Locate every blood parasite and identify its species.
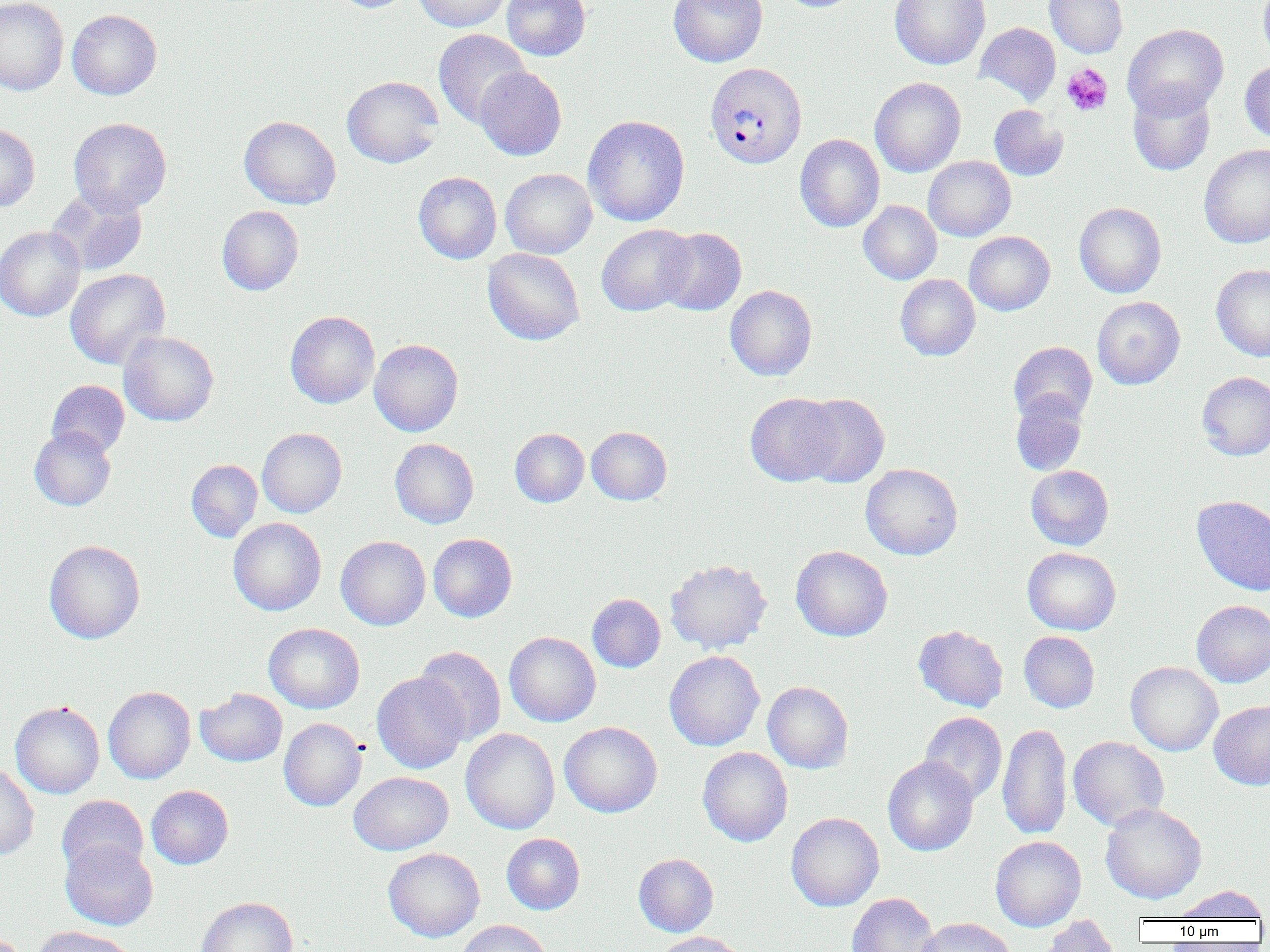

Approximate bounding boxes as named x1/y1/x2/y2 corners in pixels.
Plasmodium vivax-infected red blood cells: (x1=704, y1=62, x2=807, y2=170).
No Plasmodium falciparum, Plasmodium ovale, Plasmodium malariae, Babesia divergens, or Trypanosoma brucei observed.

slide-level diagnosis = Plasmodium vivax
field of view = single
platelet locations = approximate bounding boxes as named x1/y1/x2/y2 corners in pixels: (x1=1061, y1=63, x2=1113, y2=116)
preparation = thin blood film
modality = optical microscopy
magnification = 1000x
image size = 1270×952 pixels
uninfected red blood cell locations = approximate bounding boxes as named x1/y1/x2/y2 corners in pixels: (x1=0, y1=0, x2=69, y2=95), (x1=332, y1=0, x2=414, y2=13), (x1=412, y1=0, x2=512, y2=31), (x1=502, y1=0, x2=591, y2=61), (x1=668, y1=0, x2=767, y2=67), (x1=776, y1=0, x2=862, y2=12), (x1=889, y1=0, x2=991, y2=70), (x1=1044, y1=0, x2=1128, y2=58), (x1=1258, y1=0, x2=1270, y2=67), (x1=66, y1=9, x2=162, y2=100), (x1=974, y1=22, x2=1060, y2=105), (x1=1122, y1=24, x2=1228, y2=119), (x1=433, y1=29, x2=531, y2=128), (x1=1240, y1=60, x2=1270, y2=144), (x1=474, y1=67, x2=567, y2=160), (x1=342, y1=76, x2=444, y2=168), (x1=870, y1=77, x2=966, y2=177), (x1=1128, y1=84, x2=1216, y2=176), (x1=989, y1=105, x2=1068, y2=181), (x1=582, y1=115, x2=690, y2=226), (x1=239, y1=116, x2=341, y2=209), (x1=68, y1=117, x2=172, y2=216), (x1=0, y1=123, x2=40, y2=211), (x1=795, y1=133, x2=885, y2=232), (x1=1199, y1=144, x2=1270, y2=248), (x1=923, y1=156, x2=1016, y2=241), (x1=500, y1=168, x2=597, y2=259), (x1=413, y1=172, x2=502, y2=264), (x1=47, y1=186, x2=147, y2=277), (x1=858, y1=200, x2=942, y2=284), (x1=1074, y1=202, x2=1167, y2=298), (x1=217, y1=205, x2=304, y2=295), (x1=596, y1=224, x2=695, y2=316), (x1=0, y1=226, x2=85, y2=321), (x1=657, y1=227, x2=747, y2=315), (x1=964, y1=231, x2=1055, y2=315), (x1=483, y1=247, x2=585, y2=345), (x1=1211, y1=264, x2=1270, y2=362), (x1=65, y1=269, x2=170, y2=369), (x1=895, y1=274, x2=980, y2=361), (x1=725, y1=285, x2=817, y2=381), (x1=1092, y1=296, x2=1185, y2=389), (x1=285, y1=311, x2=379, y2=408), (x1=119, y1=331, x2=219, y2=426), (x1=369, y1=339, x2=464, y2=436), (x1=1008, y1=341, x2=1097, y2=425), (x1=1197, y1=372, x2=1270, y2=460), (x1=46, y1=380, x2=130, y2=458), (x1=745, y1=392, x2=845, y2=486), (x1=1010, y1=393, x2=1088, y2=476), (x1=795, y1=394, x2=890, y2=488), (x1=29, y1=426, x2=116, y2=511), (x1=587, y1=426, x2=672, y2=504), (x1=257, y1=428, x2=346, y2=517), (x1=510, y1=428, x2=589, y2=507), (x1=390, y1=438, x2=479, y2=529), (x1=186, y1=459, x2=262, y2=542), (x1=860, y1=463, x2=963, y2=560), (x1=1025, y1=465, x2=1114, y2=550), (x1=1192, y1=496, x2=1270, y2=596), (x1=228, y1=517, x2=326, y2=616), (x1=428, y1=533, x2=517, y2=622), (x1=336, y1=536, x2=431, y2=630), (x1=43, y1=540, x2=145, y2=644), (x1=790, y1=545, x2=893, y2=641), (x1=1022, y1=547, x2=1121, y2=635), (x1=665, y1=559, x2=772, y2=654), (x1=587, y1=594, x2=665, y2=672), (x1=1191, y1=600, x2=1270, y2=687), (x1=264, y1=623, x2=364, y2=713), (x1=913, y1=625, x2=1008, y2=712), (x1=1018, y1=631, x2=1100, y2=712), (x1=504, y1=632, x2=601, y2=727), (x1=415, y1=646, x2=506, y2=745), (x1=664, y1=650, x2=765, y2=751), (x1=1125, y1=661, x2=1223, y2=756), (x1=372, y1=672, x2=469, y2=774), (x1=763, y1=681, x2=853, y2=773), (x1=103, y1=686, x2=196, y2=784), (x1=195, y1=688, x2=287, y2=767), (x1=1209, y1=700, x2=1270, y2=790), (x1=10, y1=701, x2=104, y2=798), (x1=919, y1=712, x2=1008, y2=805), (x1=278, y1=718, x2=366, y2=811), (x1=559, y1=721, x2=662, y2=818), (x1=997, y1=722, x2=1072, y2=840), (x1=460, y1=728, x2=560, y2=835), (x1=1068, y1=736, x2=1169, y2=831), (x1=697, y1=746, x2=793, y2=846), (x1=883, y1=756, x2=979, y2=856), (x1=0, y1=764, x2=39, y2=861), (x1=348, y1=771, x2=453, y2=855), (x1=146, y1=785, x2=233, y2=869), (x1=57, y1=795, x2=148, y2=878), (x1=1100, y1=803, x2=1206, y2=904), (x1=786, y1=812, x2=884, y2=911), (x1=501, y1=833, x2=585, y2=914), (x1=990, y1=835, x2=1086, y2=931), (x1=60, y1=839, x2=158, y2=930), (x1=383, y1=848, x2=485, y2=942), (x1=633, y1=853, x2=719, y2=936), (x1=1171, y1=885, x2=1268, y2=922), (x1=846, y1=892, x2=940, y2=952), (x1=196, y1=897, x2=298, y2=952), (x1=1038, y1=915, x2=1121, y2=952), (x1=916, y1=917, x2=1016, y2=952), (x1=456, y1=920, x2=552, y2=952), (x1=31, y1=926, x2=136, y2=952), (x1=651, y1=931, x2=748, y2=952)